Locate Plasmodium parasites and leukocytes.
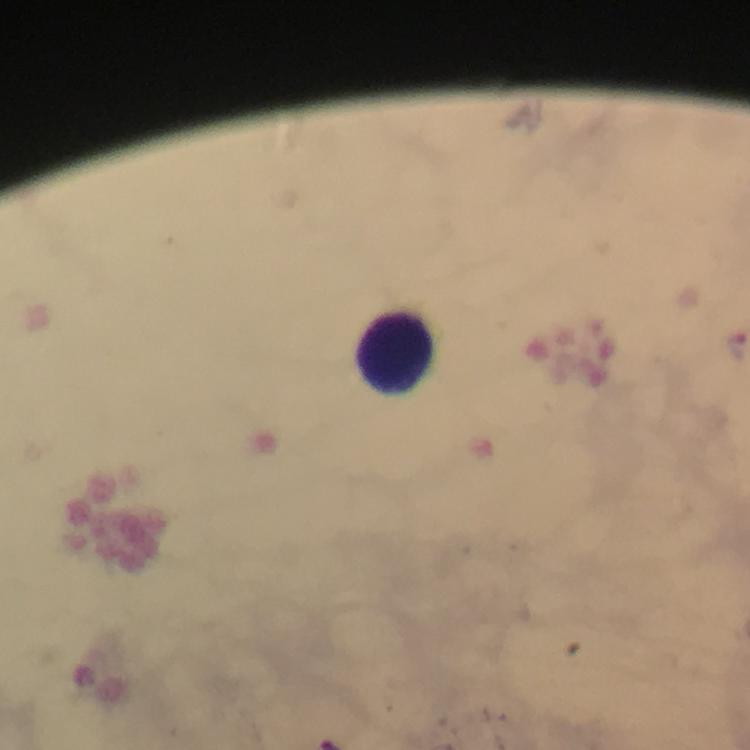

No Plasmodium parasites detected.
Approximate centers as [x, y] in pixels.
Leukocytes: [400, 351].

Summary:
  - Magnification: 100x
  - Stain: Giemsa
  - Immersion oil: applied
  - Preparation: thick smear
  - Image size: 750×750 pixels
  - Capture: smartphone camera through the microscope
  - Context: from a diagnostic examination for malaria
  - Cropped from: a single field of view